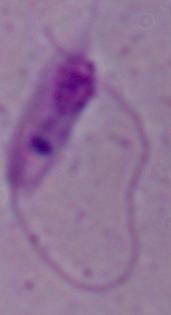 Captured at 1000x magnification. Micrograph. A Leishmania parasite is shown.